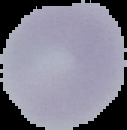
Image is 127×130 pixels. Malaria status: uninfected. From a thin blood smear. Cell region segmented out of the field of view; the surrounding area is masked to black.